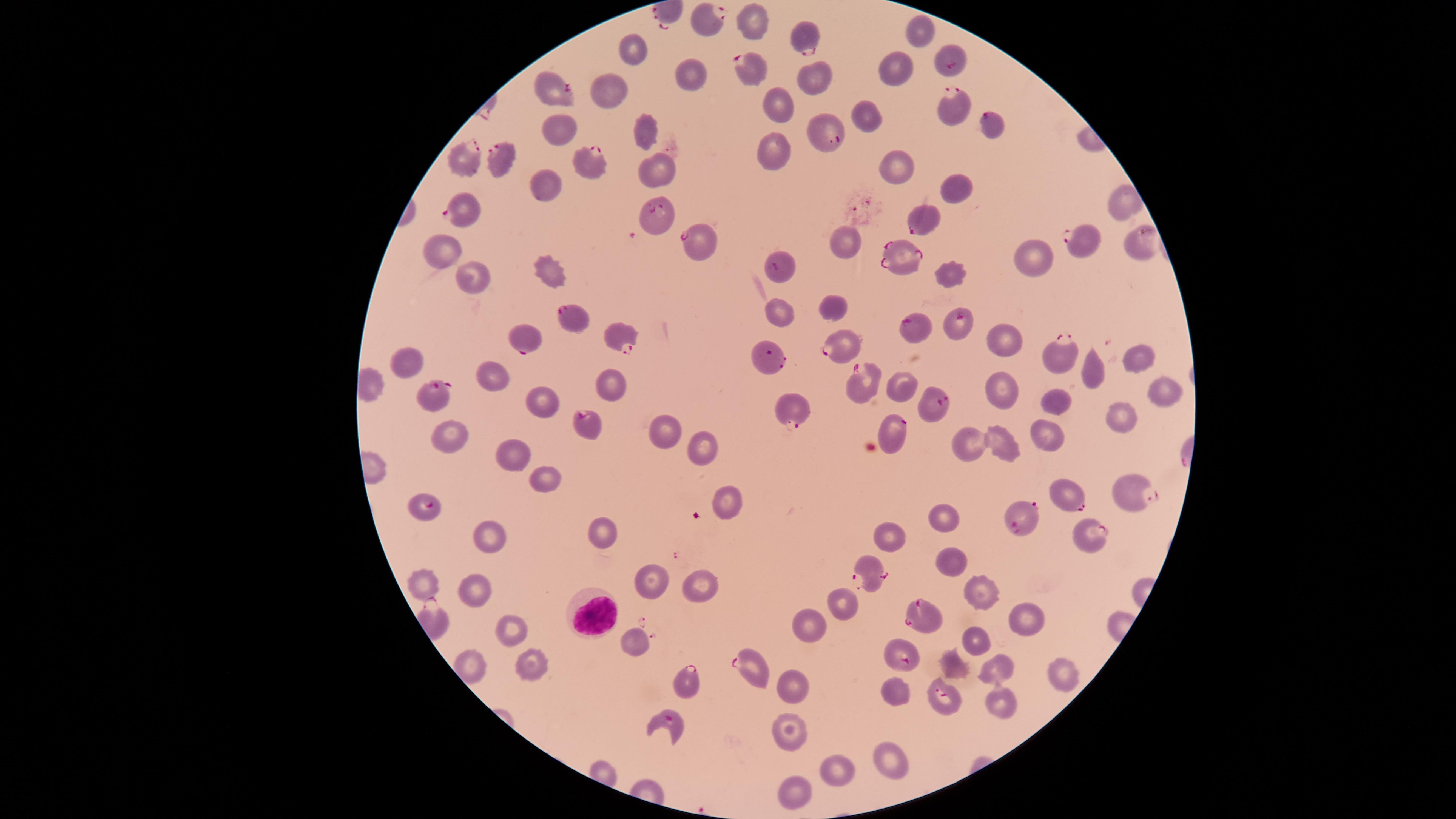
stain = Giemsa
image size = 1456×819 pixels
capture = smartphone photograph through the microscope eyepiece
WBCs = approximate marker points as [x, y] in pixels: [592, 614]
presence = malaria parasites detected
visible region = circular
uninfected RBCs = approximate marker points as [x, y] in pixels: [754, 23], [921, 26], [631, 51], [901, 66], [692, 77], [816, 83], [608, 89], [777, 108], [871, 118], [644, 122], [558, 130], [773, 151], [899, 167], [662, 169], [547, 185], [953, 188], [1122, 203], [842, 241], [443, 251], [1031, 259], [950, 269], [549, 270], [470, 278], [833, 306], [780, 307], [1005, 336], [1139, 357], [405, 360], [492, 374], [1088, 375], [608, 382], [901, 382], [1000, 386], [1165, 387], [539, 396], [1058, 403], [1121, 416], [1048, 428], [665, 429], [449, 431], [1004, 439], [963, 441], [701, 447], [509, 453], [536, 476], [731, 500], [944, 513], [599, 534], [489, 536], [891, 539], [951, 558], [425, 581], [650, 582], [697, 587], [473, 588], [987, 589], [842, 598], [1027, 614], [808, 625], [511, 629], [633, 639], [975, 639], [951, 660], [533, 661], [471, 669], [996, 673], [1062, 673], [792, 684], [895, 691], [1001, 703], [787, 728], [884, 755], [840, 767], [794, 788]
preparation = thin smear of blood
parasitized RBCs = approximate marker points as [x, y] in pixels: [708, 20], [809, 37], [953, 61], [751, 63], [555, 85], [950, 107], [991, 123], [824, 132], [502, 156], [466, 158], [594, 160], [461, 207], [654, 213], [930, 216], [1077, 237], [699, 241], [1145, 241], [900, 251], [776, 266], [574, 320], [958, 321], [916, 327], [612, 332], [523, 336], [840, 345], [1056, 356], [769, 357], [862, 383], [427, 392], [927, 404], [791, 412], [587, 419], [895, 435], [1072, 492], [1130, 492], [423, 506], [1021, 520], [1090, 533], [873, 573], [924, 616], [900, 655], [752, 667], [685, 681], [942, 694], [670, 721]
field of view = single
species = Plasmodium falciparum